Classify this cell by malaria status.
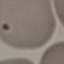

Uninfected.

stain = Giemsa
image type = automatically extracted cell patch, resized to 64 × 64 pixels
capture = smartphone through the microscope eyepiece
preparation = thin smear